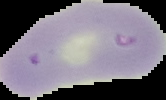
Summary:
  - Malaria status: uninfected
  - Preparation: thin blood smear
  - Image type: cell region segmented out of the field of view; surrounding area masked to black
  - Image size: 166×100 pixels